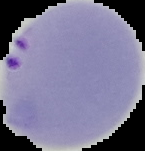

Summary:
  - Preparation: thin blood film
  - Image size: 145×151 pixels
  - Image type: segmented cell region with the area outside set to black
  - Result: Plasmodium parasites detected